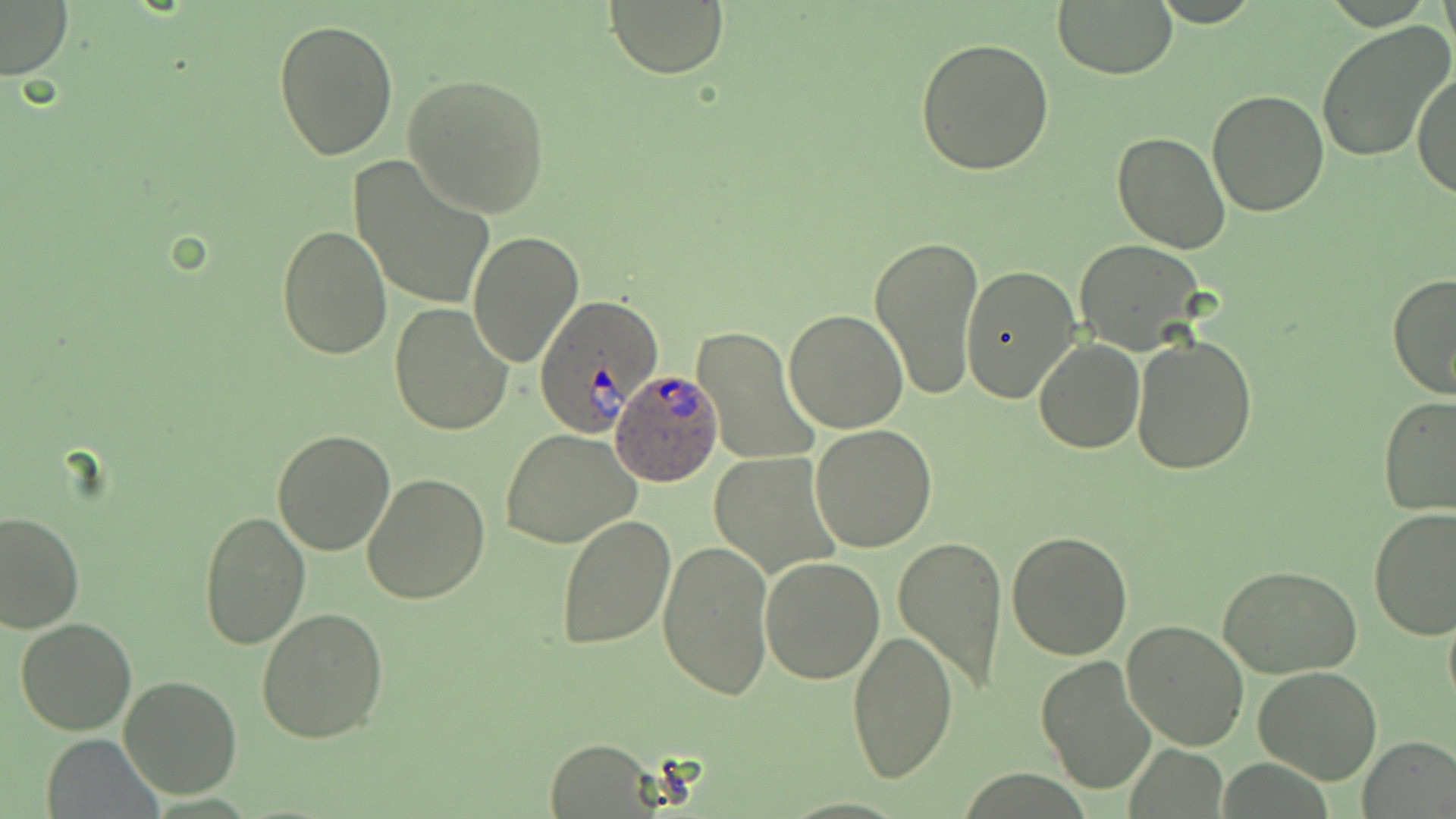
Approximate bounding boxes as named x1/y1/x2/y2 corners in pixels. Plasmodium ovale-infected red blood cell locations: (x1=533, y1=296, x2=663, y2=437), (x1=609, y1=368, x2=724, y2=487). Uninfected red blood cell locations: (x1=605, y1=0, x2=728, y2=79), (x1=1439, y1=0, x2=1455, y2=57), (x1=0, y1=2, x2=73, y2=82), (x1=1053, y1=2, x2=1177, y2=79), (x1=274, y1=18, x2=399, y2=159), (x1=1318, y1=21, x2=1452, y2=161), (x1=916, y1=36, x2=1054, y2=177), (x1=1414, y1=68, x2=1455, y2=197), (x1=403, y1=72, x2=551, y2=219), (x1=1206, y1=88, x2=1330, y2=217), (x1=1113, y1=132, x2=1232, y2=256), (x1=351, y1=155, x2=494, y2=311), (x1=291, y1=180, x2=457, y2=331), (x1=276, y1=225, x2=392, y2=359), (x1=870, y1=232, x2=984, y2=401), (x1=468, y1=233, x2=583, y2=366), (x1=1073, y1=238, x2=1206, y2=354), (x1=959, y1=265, x2=1081, y2=403), (x1=1386, y1=271, x2=1456, y2=401), (x1=388, y1=301, x2=513, y2=435), (x1=784, y1=307, x2=909, y2=431), (x1=691, y1=326, x2=817, y2=468), (x1=1131, y1=335, x2=1257, y2=475), (x1=1033, y1=338, x2=1144, y2=453), (x1=1378, y1=396, x2=1456, y2=517), (x1=808, y1=424, x2=938, y2=553), (x1=271, y1=428, x2=396, y2=556), (x1=501, y1=429, x2=641, y2=549), (x1=708, y1=453, x2=839, y2=578), (x1=363, y1=474, x2=491, y2=607), (x1=1367, y1=507, x2=1456, y2=640), (x1=199, y1=508, x2=310, y2=651), (x1=0, y1=509, x2=84, y2=632), (x1=553, y1=514, x2=674, y2=650), (x1=1006, y1=531, x2=1134, y2=661), (x1=893, y1=533, x2=1009, y2=695), (x1=657, y1=539, x2=773, y2=701), (x1=760, y1=555, x2=886, y2=683), (x1=1218, y1=564, x2=1362, y2=678), (x1=1442, y1=602, x2=1456, y2=715), (x1=255, y1=606, x2=388, y2=743), (x1=15, y1=618, x2=137, y2=735), (x1=1121, y1=620, x2=1250, y2=751), (x1=846, y1=629, x2=958, y2=783), (x1=1035, y1=654, x2=1157, y2=794), (x1=1253, y1=666, x2=1384, y2=783), (x1=121, y1=674, x2=243, y2=800), (x1=1360, y1=735, x2=1456, y2=818), (x1=41, y1=736, x2=163, y2=819), (x1=543, y1=737, x2=662, y2=816). Slide-level diagnosis: Plasmodium ovale. 1000x magnification. Image is 1456×819 pixels. Thin blood film. One field of a larger specimen. Optical microscopy. May-Grünwald-Giemsa stain.